Assess this cell for malaria.
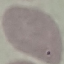

Uninfected.

Acquired by smartphone through the microscope eyepiece. Thin blood film. Automatically extracted cell patch, resized to 64 × 64 pixels. Giemsa stain.